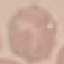 Result: no malaria parasites seen. Giemsa stain. Acquired by smartphone through the microscope eyepiece. Thin smear of blood. Cell patch, automatically extracted from a larger field of view and resized to 64 × 64 pixels.